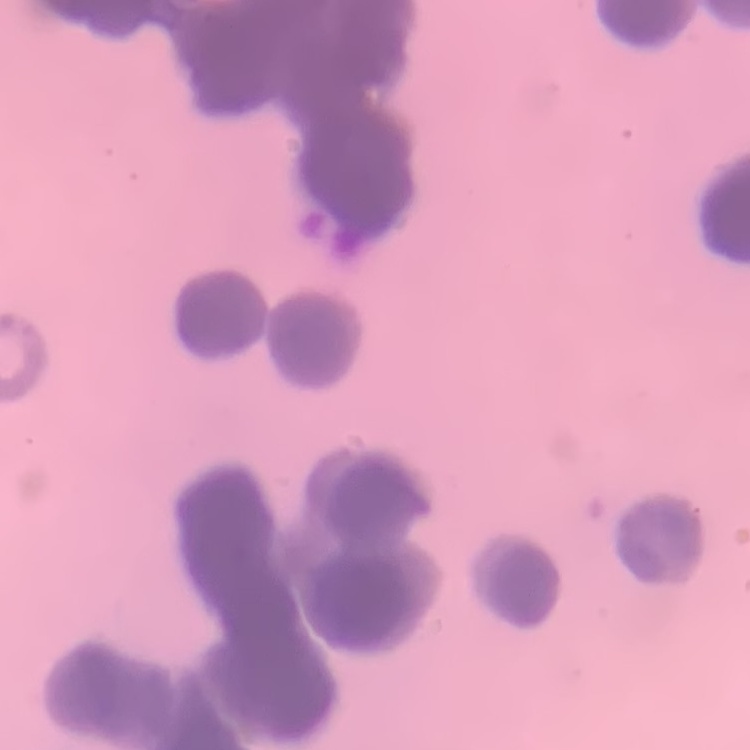

{
  "erythrocyte_morphology": "rouleaux formation",
  "preparation": "thin peripheral smear",
  "stain": "Field's or Giemsa",
  "image_type": "one tile cut from a larger photomicrograph"
}